Identify the parasite.
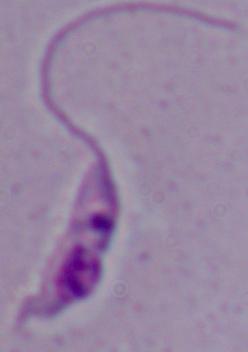
This is Leishmania.

magnification = 1000x
modality = photomicrograph